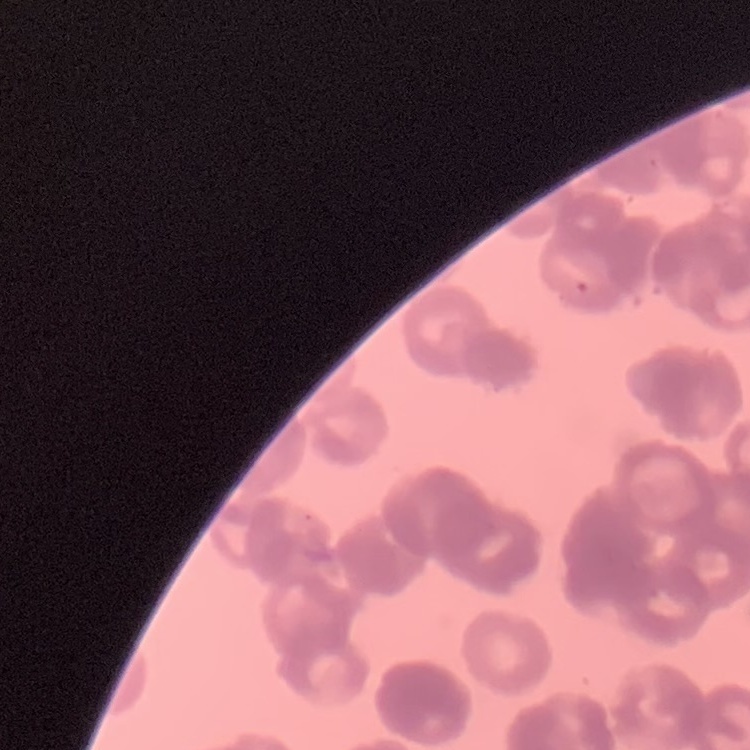

red blood cell morphology = rouleaux formation
stain = Field's or Giemsa
image type = square crop of a larger photomicrograph
preparation = thin blood film